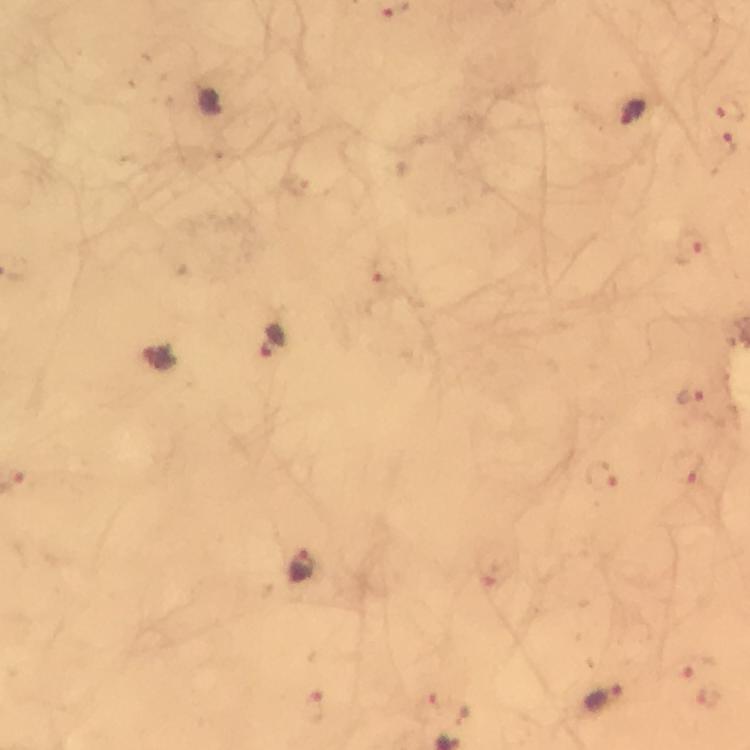
{
  "malaria_parasite_locations": "approximate centers as (x, y) in pixels: (633, 113), (724, 143), (692, 243), (383, 273), (271, 341), (160, 357), (692, 397), (685, 467), (605, 476), (303, 568), (488, 582), (697, 667), (605, 697), (711, 699), (314, 709), (426, 709)",
  "cropped_from": "a single field of view",
  "preparation": "thick smear",
  "capture": "smartphone camera through the microscope",
  "image_size": "750×750 pixels",
  "immersion_oil": "used",
  "context": "from a malaria diagnostic workup",
  "stain": "Giemsa",
  "magnification": "100x"
}